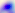
identification = Toxoplasma gondii
modality = micrograph
magnification = 400x